Describe the morphology of the red blood cells.
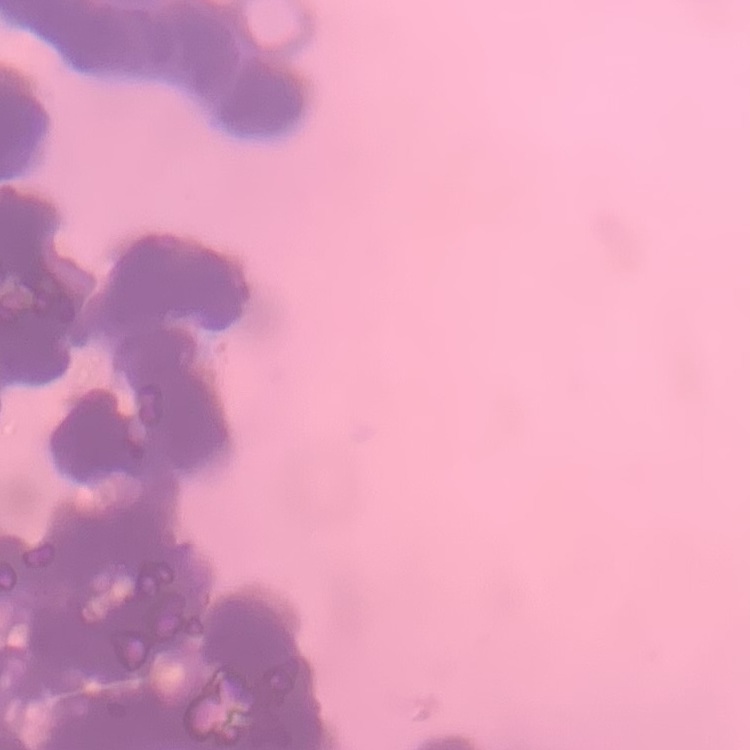

They show rouleaux formation.

Summary:
  - Stain: Field's or Giemsa
  - Preparation: thin peripheral smear
  - Image type: square crop of a larger photomicrograph